Identify the cell.
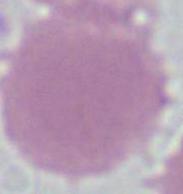

An erythrocyte.

magnification = 1000x
modality = micrograph